Classify this cell by malaria status.
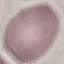

It is uninfected.

Summary:
  - Capture: smartphone through the microscope eyepiece
  - Stain: Giemsa
  - Image type: automatically extracted cell patch, resized to 64 × 64 pixels
  - Preparation: thin smear